Assess the morphology of the erythrocytes.
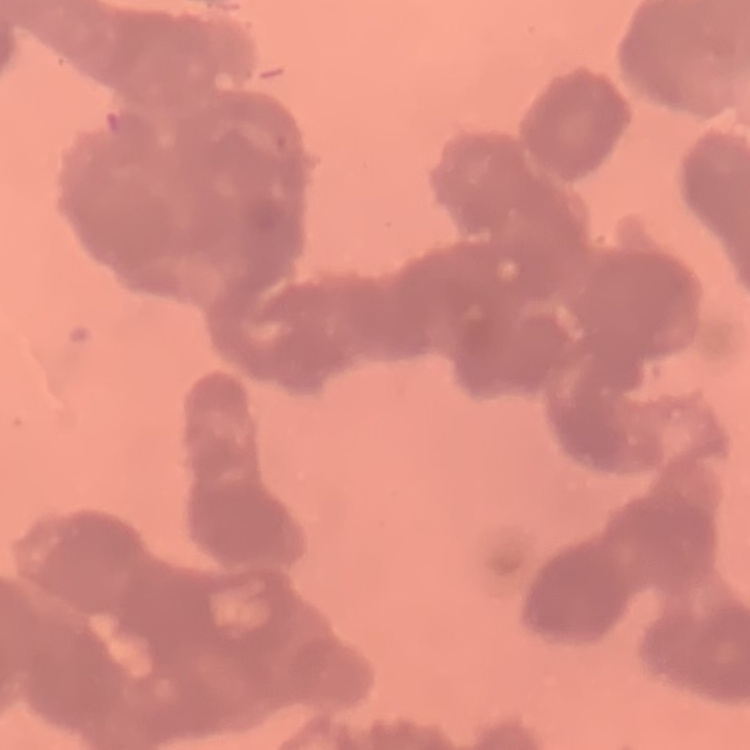

They show rouleaux formation.

stain = Field's or Giemsa
preparation = thin blood smear
image type = square crop of a larger photomicrograph